Report the malaria status of this cell.
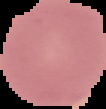
Uninfected.

The area outside the segmented cell region is set to black. Image is 106×109 pixels. From a thin blood smear.